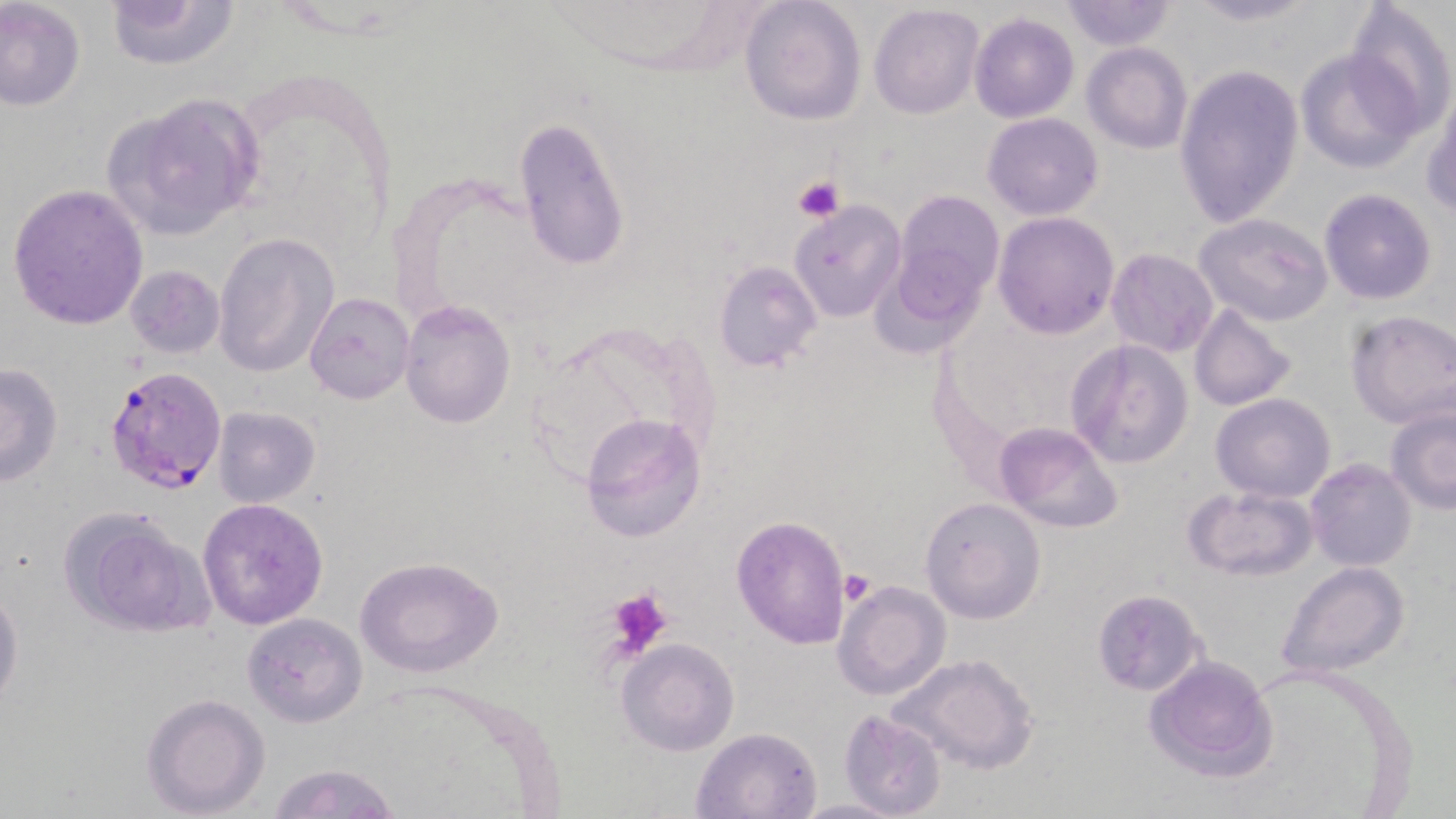 Approximate bounding boxes as (x1,y1)-(x2,y2) corner pairs in pixels. Platelet locations: (792,176)-(844,224), (837,570)-(876,607), (604,587)-(674,655). Plasmodium falciparum-infected red blood cell locations: (108,365)-(226,497). Uninfected red blood cell locations: (106,0)-(238,71), (739,0)-(867,125), (1178,0)-(1324,27), (1,1)-(85,111), (1057,1)-(1180,52), (1342,1)-(1456,140), (867,3)-(985,119), (970,15)-(1079,123), (1081,42)-(1192,154), (1295,49)-(1422,173), (1175,64)-(1304,231), (1423,83)-(1456,223), (106,92)-(266,238), (981,112)-(1104,221), (512,116)-(632,272), (5,183)-(151,330), (892,188)-(1006,319), (1318,189)-(1438,306), (790,200)-(906,322), (993,211)-(1120,339), (1193,213)-(1333,326), (212,232)-(339,379), (1105,248)-(1220,358), (713,260)-(822,372), (123,265)-(225,362), (303,291)-(414,404), (400,299)-(517,429), (1187,303)-(1298,412), (1345,311)-(1456,428), (1066,338)-(1193,469), (520,346)-(655,490), (1,361)-(64,488), (1210,393)-(1336,503), (1385,402)-(1456,515), (213,404)-(322,508), (579,411)-(707,542), (995,422)-(1122,534), (1305,459)-(1416,570), (1183,485)-(1318,581), (919,495)-(1046,626), (198,497)-(328,629), (62,507)-(214,638), (732,514)-(852,648), (355,556)-(503,678), (1276,561)-(1409,679), (831,579)-(952,702), (0,586)-(24,712), (1092,588)-(1209,697), (242,613)-(367,727), (615,637)-(741,756), (887,652)-(1039,776), (1141,653)-(1281,782), (141,692)-(271,817), (837,709)-(947,818), (691,726)-(823,817), (266,762)-(403,819), (790,796)-(905,818). Slide-level diagnosis: Plasmodium falciparum. Light microscopy. Image is 1456×819 pixels. One field of a larger specimen. Thin blood film. Captured at 1000x magnification. May-Grünwald-Giemsa stain.